Name the blood parasite species.
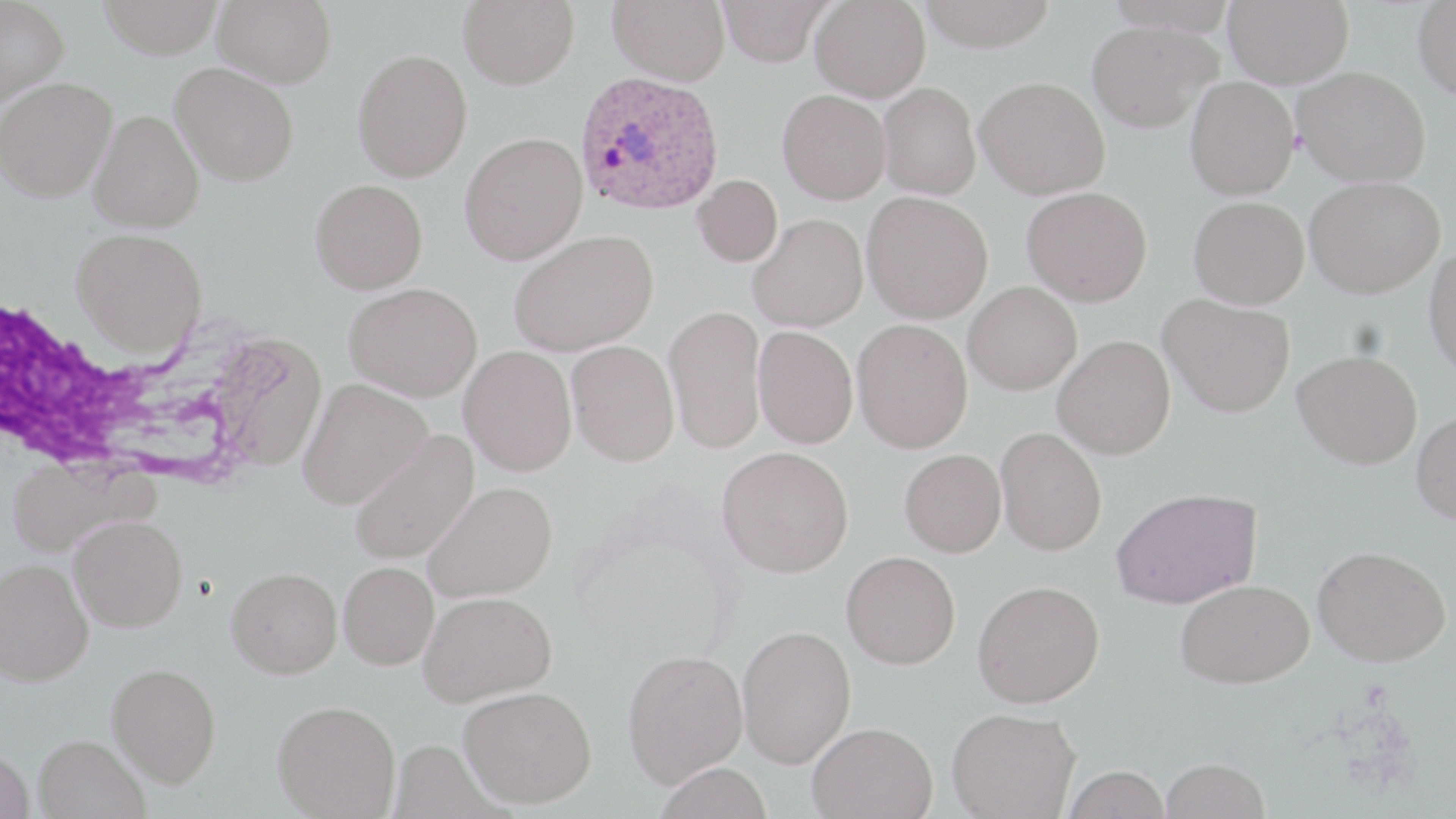
Plasmodium ovale.

Summary:
  - Coordinate format: approximate bounding boxes as named x1/y1/x2/y2 corners in pixels
  - Plasmodium ovale-infected red blood cell locations: (x1=575, y1=71, x2=724, y2=216)
  - Uninfected red blood cell locations: (x1=0, y1=0, x2=70, y2=109), (x1=98, y1=0, x2=223, y2=59), (x1=212, y1=0, x2=336, y2=88), (x1=458, y1=0, x2=579, y2=89), (x1=608, y1=0, x2=730, y2=85), (x1=717, y1=0, x2=833, y2=67), (x1=810, y1=0, x2=931, y2=102), (x1=916, y1=0, x2=1058, y2=52), (x1=1223, y1=0, x2=1354, y2=88), (x1=1412, y1=2, x2=1456, y2=99), (x1=1086, y1=20, x2=1221, y2=132), (x1=352, y1=49, x2=472, y2=182), (x1=170, y1=63, x2=299, y2=185), (x1=1293, y1=66, x2=1431, y2=186), (x1=975, y1=76, x2=1110, y2=199), (x1=1185, y1=76, x2=1299, y2=200), (x1=0, y1=77, x2=117, y2=202), (x1=878, y1=82, x2=981, y2=200), (x1=777, y1=89, x2=891, y2=204), (x1=89, y1=109, x2=204, y2=233), (x1=459, y1=132, x2=587, y2=264), (x1=693, y1=174, x2=782, y2=267), (x1=1304, y1=176, x2=1444, y2=298), (x1=310, y1=179, x2=428, y2=294), (x1=1022, y1=186, x2=1152, y2=306), (x1=862, y1=191, x2=993, y2=323), (x1=1189, y1=196, x2=1309, y2=308), (x1=748, y1=214, x2=868, y2=332), (x1=72, y1=228, x2=207, y2=357), (x1=509, y1=230, x2=657, y2=356), (x1=1424, y1=243, x2=1456, y2=382), (x1=344, y1=282, x2=483, y2=401), (x1=964, y1=282, x2=1082, y2=395), (x1=1159, y1=294, x2=1296, y2=416), (x1=664, y1=305, x2=766, y2=453), (x1=852, y1=318, x2=973, y2=453), (x1=753, y1=326, x2=859, y2=448), (x1=207, y1=332, x2=328, y2=471), (x1=1053, y1=335, x2=1175, y2=459), (x1=567, y1=340, x2=679, y2=466), (x1=459, y1=345, x2=577, y2=475), (x1=1293, y1=350, x2=1422, y2=469), (x1=298, y1=378, x2=432, y2=508), (x1=1411, y1=410, x2=1456, y2=525), (x1=996, y1=426, x2=1107, y2=555), (x1=349, y1=430, x2=480, y2=566), (x1=718, y1=446, x2=854, y2=577), (x1=899, y1=449, x2=1006, y2=556), (x1=424, y1=482, x2=557, y2=601), (x1=1111, y1=487, x2=1261, y2=609), (x1=69, y1=515, x2=187, y2=631), (x1=1313, y1=545, x2=1451, y2=666), (x1=841, y1=551, x2=960, y2=669), (x1=0, y1=558, x2=93, y2=685), (x1=339, y1=561, x2=439, y2=669), (x1=227, y1=568, x2=342, y2=678), (x1=1176, y1=579, x2=1313, y2=688), (x1=973, y1=580, x2=1105, y2=707), (x1=419, y1=590, x2=556, y2=705), (x1=736, y1=625, x2=856, y2=768), (x1=622, y1=648, x2=748, y2=787), (x1=107, y1=663, x2=221, y2=787), (x1=458, y1=686, x2=597, y2=808), (x1=273, y1=700, x2=401, y2=819), (x1=947, y1=707, x2=1080, y2=819), (x1=807, y1=721, x2=938, y2=819), (x1=34, y1=734, x2=149, y2=819), (x1=0, y1=749, x2=34, y2=819), (x1=1160, y1=757, x2=1269, y2=819), (x1=653, y1=762, x2=773, y2=819), (x1=1061, y1=765, x2=1173, y2=819)
  - White blood cell locations: (x1=2, y1=298, x2=240, y2=483)
  - Preparation: thin blood film
  - Field of view: single
  - Magnification: 1000x
  - Image size: 1456×819 pixels
  - Modality: optical microscopy
  - Stain: May-Grünwald-Giemsa